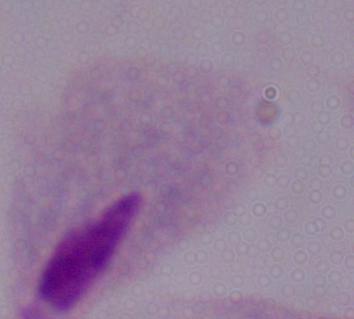

A trichomonad is shown. Photomicrograph. Captured at 1000x magnification.